Give the preparation type.
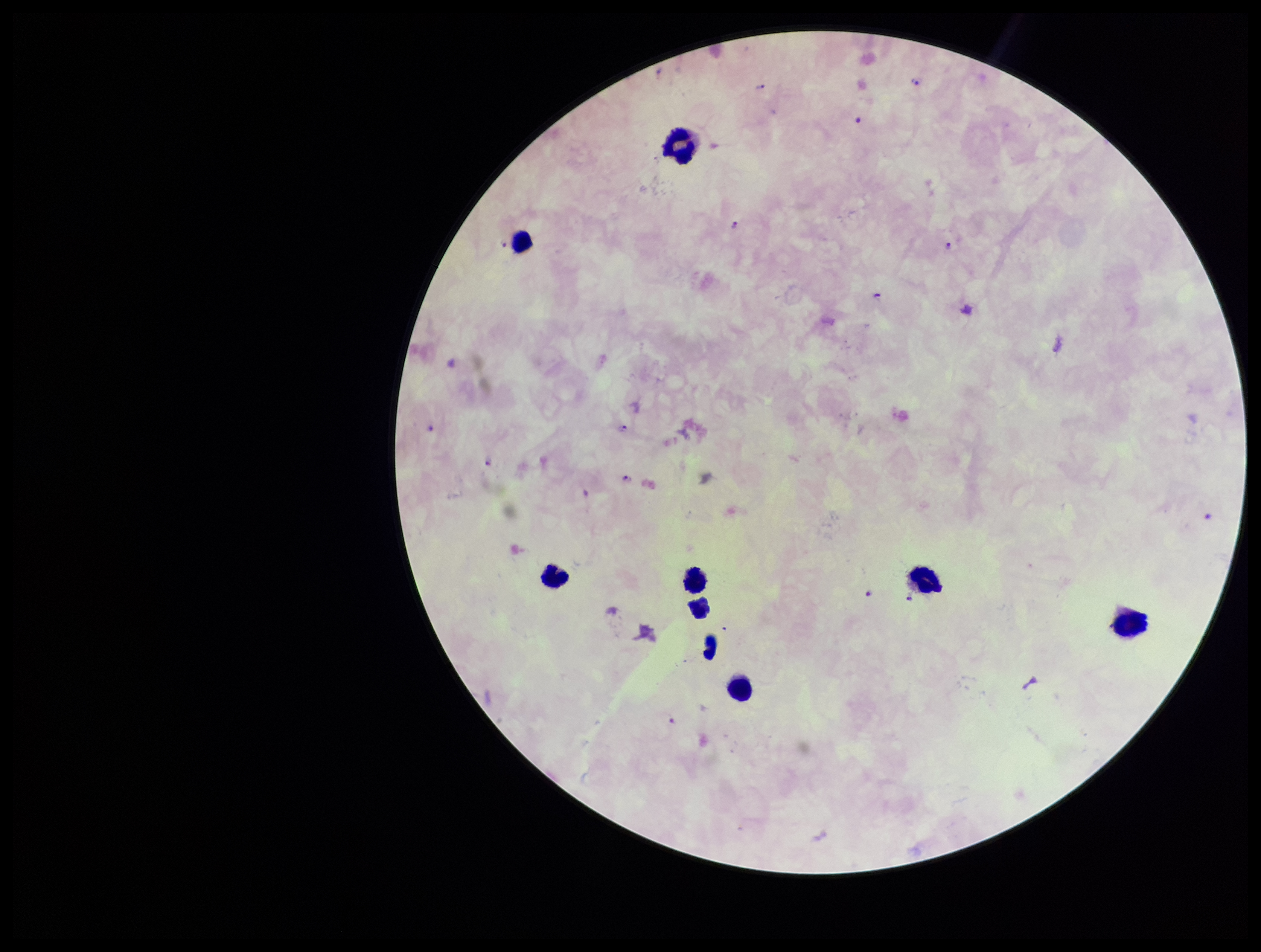
Thick.

stain = Giemsa
patient malaria status = infected
leukocyte count = 9
Plasmodium parasites = identified
capture = smartphone photograph through the microscope eyepiece
parasite count = 15
image size = 1261×952 pixels
field of view = one from this slide
species reported for this patient = Plasmodium falciparum